Locate every Trypanosoma brucei.
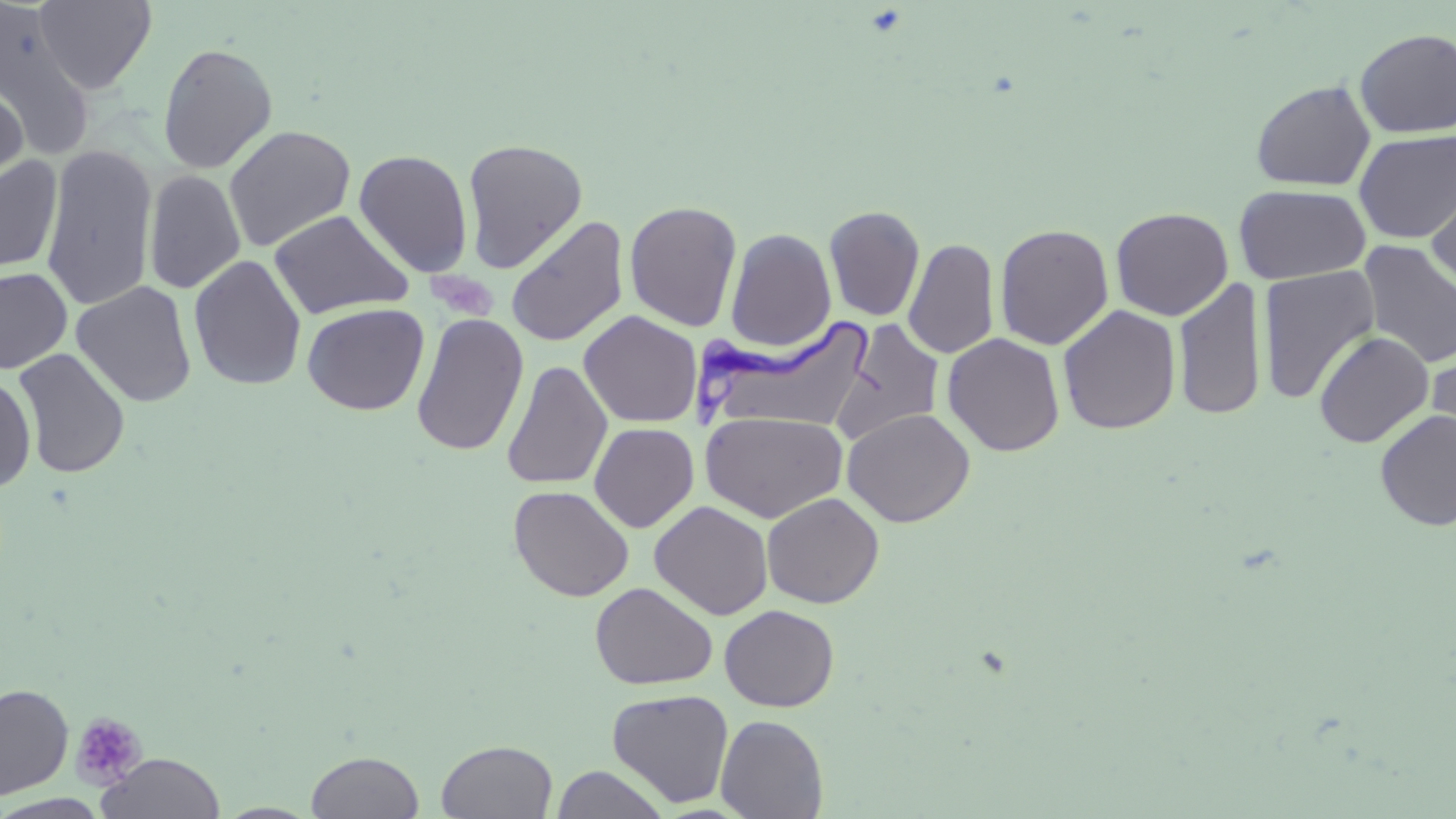
Approximate bounding boxes as named x1/y1/x2/y2 corners in pixels.
Trypanosoma brucei: (x1=698, y1=316, x2=875, y2=433).

Summary:
  - Platelet locations: (x1=423, y1=265, x2=502, y2=322), (x1=71, y1=711, x2=146, y2=789)
  - Uninfected red blood cell locations: (x1=35, y1=0, x2=157, y2=93), (x1=0, y1=5, x2=96, y2=159), (x1=1354, y1=28, x2=1456, y2=138), (x1=157, y1=42, x2=278, y2=174), (x1=1251, y1=79, x2=1375, y2=191), (x1=0, y1=82, x2=28, y2=200), (x1=222, y1=125, x2=357, y2=252), (x1=1354, y1=129, x2=1456, y2=244), (x1=461, y1=138, x2=588, y2=273), (x1=41, y1=145, x2=157, y2=312), (x1=353, y1=149, x2=474, y2=278), (x1=1, y1=155, x2=63, y2=274), (x1=144, y1=169, x2=246, y2=295), (x1=1425, y1=172, x2=1456, y2=294), (x1=1234, y1=183, x2=1370, y2=284), (x1=624, y1=200, x2=742, y2=331), (x1=823, y1=205, x2=925, y2=322), (x1=1110, y1=206, x2=1234, y2=321), (x1=270, y1=209, x2=413, y2=320), (x1=505, y1=215, x2=629, y2=348), (x1=994, y1=223, x2=1114, y2=350), (x1=725, y1=227, x2=836, y2=352), (x1=904, y1=237, x2=999, y2=359), (x1=1357, y1=240, x2=1456, y2=369), (x1=188, y1=254, x2=307, y2=392), (x1=1257, y1=266, x2=1380, y2=404), (x1=0, y1=267, x2=73, y2=374), (x1=1172, y1=278, x2=1267, y2=422), (x1=71, y1=281, x2=198, y2=407), (x1=302, y1=302, x2=429, y2=415), (x1=1057, y1=304, x2=1181, y2=435), (x1=579, y1=310, x2=703, y2=428), (x1=411, y1=313, x2=529, y2=457), (x1=833, y1=317, x2=945, y2=445), (x1=1314, y1=331, x2=1434, y2=448), (x1=942, y1=333, x2=1065, y2=456), (x1=1426, y1=341, x2=1456, y2=462), (x1=12, y1=347, x2=131, y2=479), (x1=501, y1=360, x2=612, y2=489), (x1=0, y1=373, x2=36, y2=492), (x1=842, y1=408, x2=975, y2=527), (x1=1375, y1=408, x2=1456, y2=531), (x1=700, y1=410, x2=849, y2=523), (x1=589, y1=422, x2=699, y2=532), (x1=508, y1=485, x2=634, y2=602), (x1=761, y1=492, x2=884, y2=608), (x1=649, y1=500, x2=773, y2=620), (x1=590, y1=582, x2=717, y2=690), (x1=719, y1=604, x2=839, y2=712), (x1=0, y1=683, x2=74, y2=799), (x1=607, y1=688, x2=734, y2=808), (x1=715, y1=714, x2=828, y2=819), (x1=436, y1=740, x2=558, y2=818), (x1=306, y1=750, x2=424, y2=818), (x1=98, y1=752, x2=225, y2=819), (x1=550, y1=765, x2=670, y2=819), (x1=0, y1=793, x2=111, y2=818), (x1=214, y1=802, x2=321, y2=818)
  - Slide-level diagnosis: Trypanosoma brucei
  - Field of view: single
  - Preparation: thin blood film
  - Modality: optical microscopy
  - Magnification: 1000x
  - Stain: May-Grünwald-Giemsa
  - Image size: 1456×819 pixels